Describe the morphology of the erythrocytes.
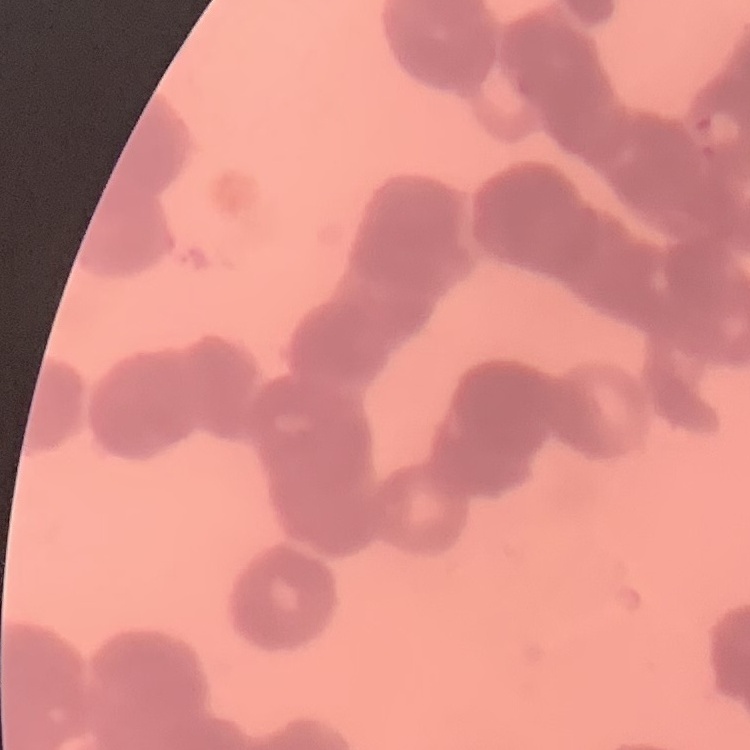
They show rouleaux formation.

Thin peripheral smear. One tile cut from a larger photomicrograph. Field's or Giemsa stain.